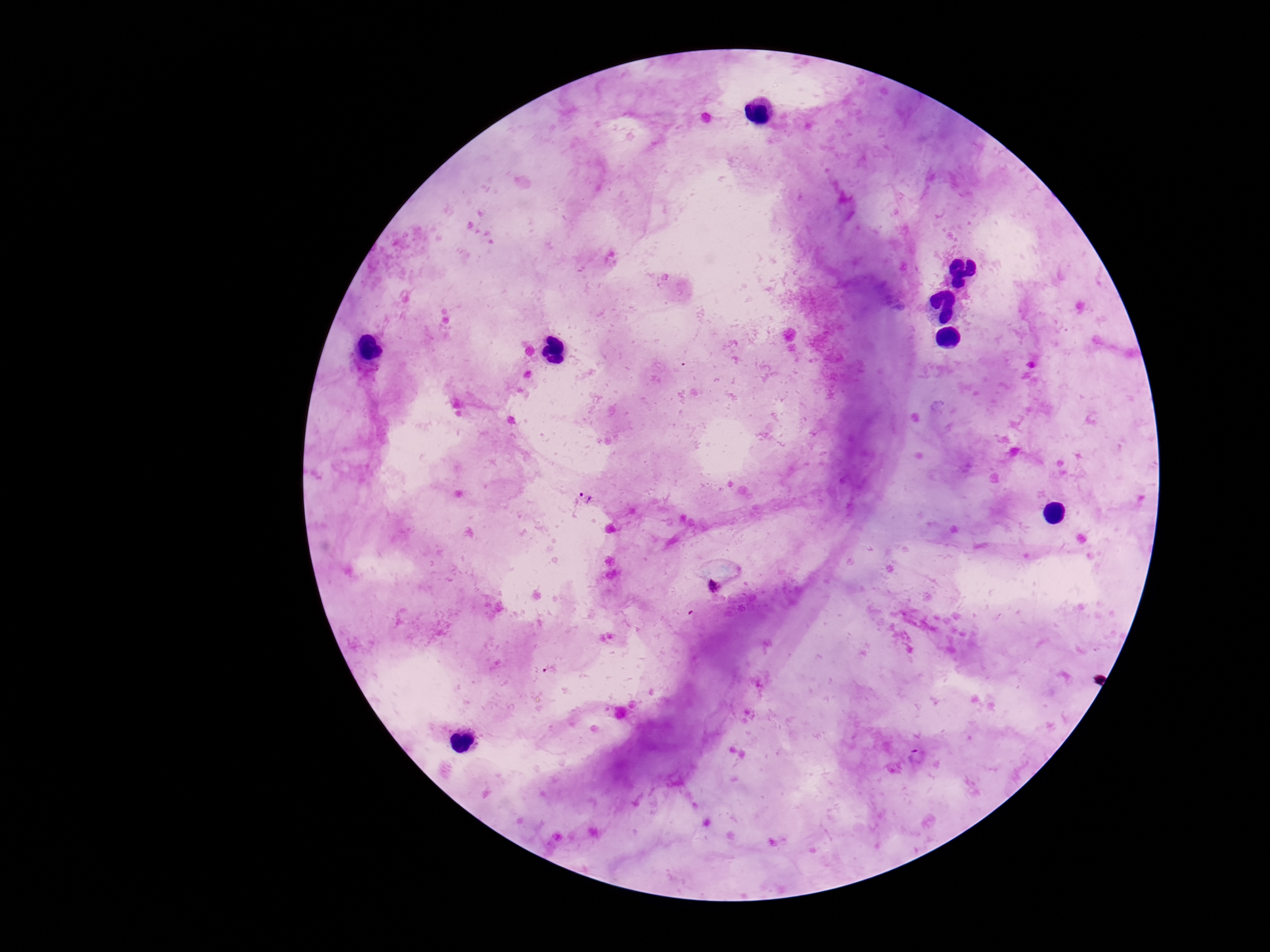
Approximate centers as {x, y} in pixels. Plasmodium parasite locations: {587, 494}, {713, 587}. 100x magnification. Image is 1270×952 pixels. Giemsa stain. One field from this slide. Photographed through the microscope eyepiece with a smartphone camera. Patient malaria status: positive. Thick blood smear.